Locate platelets.
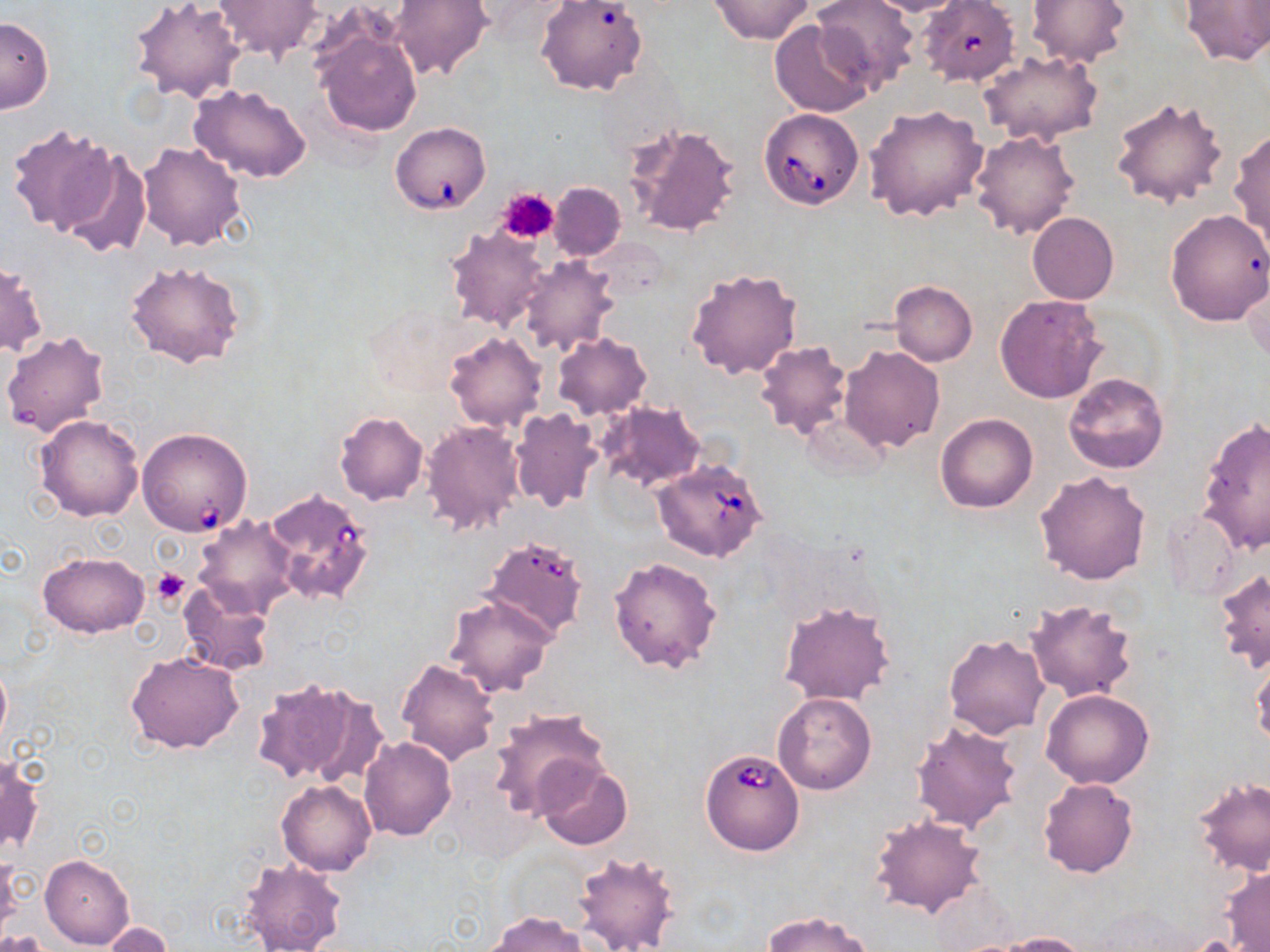
Approximate bounding boxes as named x1/y1/x2/y2 corners in pixels.
Platelets: (x1=497, y1=189, x2=558, y2=244), (x1=152, y1=568, x2=190, y2=607).

slide-level diagnosis = Babesia divergens
image size = 1270×952 pixels
stain = May-Grünwald-Giemsa
Babesia divergens-infected red blood cell locations = approximate bounding boxes as named x1/y1/x2/y2 corners in pixels: (x1=919, y1=0, x2=1019, y2=88), (x1=759, y1=108, x2=865, y2=209), (x1=390, y1=120, x2=491, y2=215), (x1=137, y1=427, x2=254, y2=536), (x1=650, y1=458, x2=768, y2=562), (x1=261, y1=485, x2=376, y2=606), (x1=482, y1=535, x2=589, y2=640), (x1=699, y1=747, x2=806, y2=856)
field of view = one of a larger specimen
preparation = thin blood film
modality = light microscopy
magnification = 1000x
uninfected red blood cell locations = approximate bounding boxes as named x1/y1/x2/y2 corners in pixels: (x1=212, y1=0, x2=324, y2=63), (x1=390, y1=0, x2=491, y2=82), (x1=710, y1=0, x2=813, y2=44), (x1=812, y1=0, x2=920, y2=95), (x1=859, y1=0, x2=971, y2=16), (x1=1025, y1=0, x2=1132, y2=69), (x1=1179, y1=0, x2=1270, y2=66), (x1=130, y1=1, x2=247, y2=104), (x1=535, y1=2, x2=648, y2=97), (x1=0, y1=15, x2=53, y2=113), (x1=311, y1=19, x2=424, y2=139), (x1=769, y1=20, x2=875, y2=118), (x1=976, y1=50, x2=1104, y2=146), (x1=188, y1=84, x2=313, y2=184), (x1=1110, y1=96, x2=1229, y2=210), (x1=865, y1=104, x2=990, y2=223), (x1=626, y1=121, x2=740, y2=239), (x1=6, y1=123, x2=118, y2=238), (x1=969, y1=129, x2=1080, y2=240), (x1=1229, y1=129, x2=1270, y2=244), (x1=137, y1=141, x2=247, y2=250), (x1=57, y1=147, x2=152, y2=260), (x1=549, y1=182, x2=626, y2=260), (x1=1165, y1=209, x2=1270, y2=327), (x1=1028, y1=212, x2=1119, y2=305), (x1=444, y1=226, x2=551, y2=333), (x1=516, y1=255, x2=619, y2=357), (x1=1, y1=256, x2=49, y2=357), (x1=123, y1=258, x2=246, y2=368), (x1=686, y1=267, x2=802, y2=380), (x1=1238, y1=270, x2=1269, y2=362), (x1=889, y1=280, x2=977, y2=366), (x1=993, y1=294, x2=1106, y2=404), (x1=1, y1=330, x2=111, y2=438), (x1=444, y1=330, x2=547, y2=433), (x1=551, y1=333, x2=652, y2=419), (x1=754, y1=340, x2=851, y2=441), (x1=840, y1=345, x2=945, y2=452), (x1=1063, y1=372, x2=1169, y2=474), (x1=596, y1=400, x2=707, y2=491), (x1=509, y1=407, x2=604, y2=513), (x1=335, y1=411, x2=429, y2=504), (x1=935, y1=413, x2=1037, y2=513), (x1=34, y1=414, x2=145, y2=522), (x1=1197, y1=418, x2=1270, y2=553), (x1=420, y1=420, x2=525, y2=537), (x1=1035, y1=470, x2=1151, y2=586), (x1=1161, y1=510, x2=1240, y2=602), (x1=193, y1=515, x2=300, y2=617), (x1=37, y1=551, x2=148, y2=638), (x1=608, y1=556, x2=722, y2=675), (x1=1213, y1=568, x2=1269, y2=672), (x1=178, y1=582, x2=274, y2=677), (x1=443, y1=593, x2=556, y2=697), (x1=1024, y1=599, x2=1137, y2=703), (x1=777, y1=600, x2=896, y2=706), (x1=944, y1=633, x2=1049, y2=739), (x1=126, y1=650, x2=246, y2=754), (x1=1249, y1=652, x2=1269, y2=746), (x1=0, y1=657, x2=11, y2=754), (x1=395, y1=658, x2=501, y2=767), (x1=250, y1=677, x2=379, y2=786), (x1=1041, y1=689, x2=1154, y2=789), (x1=773, y1=692, x2=877, y2=795), (x1=488, y1=708, x2=608, y2=817), (x1=910, y1=720, x2=1023, y2=833), (x1=359, y1=737, x2=456, y2=841), (x1=0, y1=754, x2=43, y2=858), (x1=535, y1=758, x2=633, y2=851), (x1=1038, y1=778, x2=1139, y2=878), (x1=1192, y1=778, x2=1270, y2=877), (x1=277, y1=780, x2=377, y2=876), (x1=869, y1=814, x2=990, y2=919), (x1=572, y1=849, x2=681, y2=952), (x1=40, y1=853, x2=136, y2=949), (x1=1, y1=856, x2=21, y2=938), (x1=237, y1=856, x2=349, y2=952), (x1=1221, y1=864, x2=1270, y2=951), (x1=762, y1=911, x2=877, y2=952), (x1=487, y1=912, x2=590, y2=952), (x1=96, y1=921, x2=177, y2=950), (x1=3, y1=928, x2=56, y2=951), (x1=993, y1=931, x2=1090, y2=952)